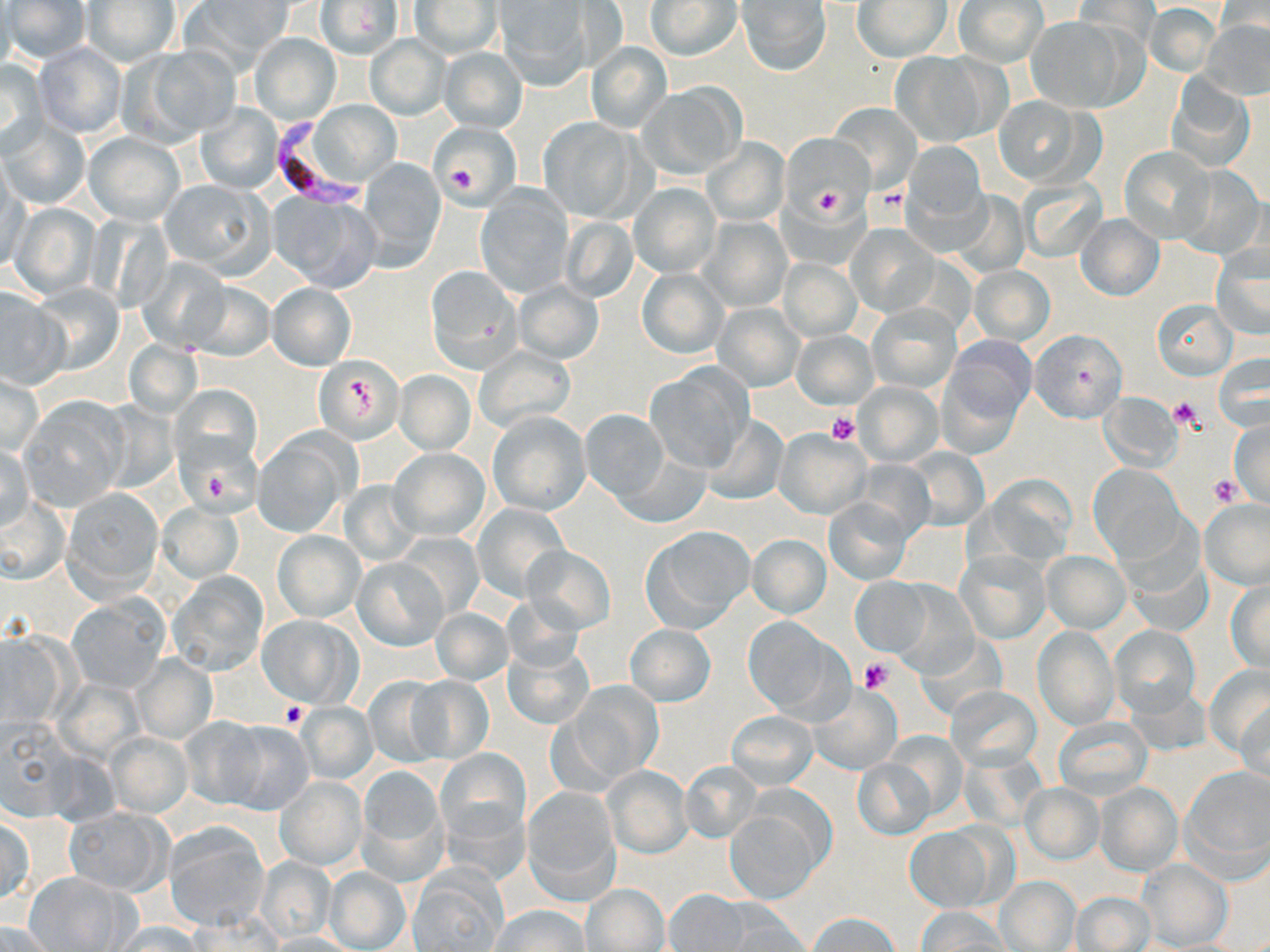 Approximate bounding boxes as [x1, y1, x2, y2] in pixels. Platelet locations: [447, 164, 477, 192], [811, 185, 846, 218], [872, 186, 910, 219], [348, 376, 373, 412], [1168, 396, 1203, 430], [826, 412, 860, 445], [203, 472, 230, 498], [1209, 474, 1243, 506], [859, 658, 893, 693], [280, 702, 308, 729]. Uninfected red blood cell locations: [5, 0, 90, 63], [186, 0, 295, 69], [645, 0, 741, 60], [737, 0, 831, 75], [315, 1, 405, 60], [409, 1, 503, 58], [494, 1, 589, 87], [853, 1, 953, 62], [953, 1, 1048, 67], [1072, 1, 1158, 60], [82, 2, 181, 67], [1144, 4, 1221, 76], [1025, 18, 1129, 112], [1201, 20, 1270, 100], [249, 34, 340, 126], [364, 35, 450, 120], [33, 42, 128, 139], [587, 42, 672, 132], [126, 46, 240, 143], [438, 48, 528, 132], [891, 50, 1006, 147], [1, 58, 49, 155], [1167, 75, 1256, 173], [637, 83, 747, 180], [993, 97, 1099, 188], [311, 101, 401, 187], [197, 103, 284, 194], [829, 106, 920, 191], [539, 117, 643, 221], [0, 119, 89, 210], [430, 121, 521, 204], [85, 132, 185, 225], [782, 134, 873, 219], [702, 136, 791, 226], [901, 141, 989, 236], [1119, 147, 1216, 243], [356, 158, 446, 270], [1169, 163, 1266, 262], [1, 171, 29, 276], [160, 179, 274, 276], [1017, 179, 1108, 261], [628, 182, 721, 279], [476, 189, 575, 298], [948, 190, 1030, 278], [269, 193, 380, 292], [8, 202, 101, 300], [1074, 214, 1164, 301], [699, 216, 793, 313], [559, 217, 639, 303], [846, 226, 940, 318], [1211, 243, 1270, 341], [136, 256, 230, 353], [779, 258, 861, 341], [969, 265, 1054, 346], [426, 267, 521, 373], [638, 269, 727, 358], [184, 280, 275, 361], [513, 281, 604, 363], [29, 282, 125, 375], [267, 282, 356, 371], [0, 286, 67, 389], [1151, 299, 1237, 379], [866, 302, 962, 394], [713, 304, 804, 391], [1028, 328, 1127, 424], [792, 331, 877, 408], [942, 335, 1036, 428], [124, 341, 202, 418], [472, 345, 577, 437], [1215, 355, 1267, 432], [314, 356, 404, 443], [644, 365, 753, 474], [394, 371, 475, 453], [0, 372, 42, 458], [854, 382, 942, 465], [1099, 391, 1182, 472], [24, 398, 126, 508], [580, 408, 670, 502], [486, 411, 590, 516], [701, 414, 788, 506], [1228, 419, 1270, 504], [774, 428, 872, 519], [253, 434, 352, 536], [1, 442, 34, 532], [614, 444, 710, 528], [902, 447, 988, 531], [388, 448, 489, 542], [1089, 465, 1185, 562], [978, 474, 1077, 567], [339, 480, 422, 566], [63, 488, 163, 596], [2, 494, 67, 583], [824, 497, 913, 584], [1198, 498, 1270, 590], [158, 502, 243, 583], [472, 503, 570, 600], [1114, 517, 1209, 634], [641, 527, 753, 631], [273, 530, 365, 622], [395, 532, 482, 620], [748, 534, 830, 618], [521, 545, 616, 634], [957, 549, 1050, 643], [1041, 550, 1130, 632], [352, 557, 447, 651], [167, 571, 269, 676], [850, 578, 932, 657], [1226, 579, 1270, 673], [68, 596, 168, 693], [431, 607, 513, 686], [257, 614, 361, 707], [742, 616, 851, 721], [626, 624, 715, 706], [1033, 626, 1119, 730], [1109, 626, 1199, 720], [503, 641, 593, 729], [132, 654, 216, 743], [1205, 665, 1269, 759], [362, 676, 450, 767], [405, 676, 493, 764], [562, 682, 663, 787], [810, 684, 902, 774], [947, 687, 1041, 770], [1235, 691, 1270, 784], [296, 702, 377, 784], [727, 710, 818, 788], [1052, 716, 1152, 801], [1, 717, 82, 818], [182, 718, 273, 808], [215, 719, 314, 816], [107, 733, 191, 817], [437, 748, 530, 842], [957, 750, 1046, 831], [852, 756, 936, 841], [679, 761, 763, 844], [604, 766, 692, 857], [1181, 766, 1268, 877], [356, 768, 444, 883], [276, 777, 366, 869], [1095, 781, 1184, 877], [522, 784, 621, 901], [1021, 784, 1102, 863], [725, 807, 822, 902], [65, 808, 170, 894], [1, 816, 34, 905], [165, 822, 270, 930], [905, 825, 1000, 913], [255, 858, 337, 941], [1136, 859, 1232, 951], [325, 867, 411, 952], [26, 871, 135, 951], [407, 873, 504, 951], [996, 877, 1081, 951], [582, 884, 669, 951], [665, 890, 753, 951], [1070, 892, 1155, 951], [702, 898, 807, 949], [492, 905, 589, 951], [916, 906, 1008, 951], [807, 911, 901, 951], [109, 921, 203, 952], [0, 922, 59, 952], [265, 932, 361, 952]. Plasmodium falciparum-infected red blood cell locations: [270, 118, 365, 209]. Slide-level diagnosis: Plasmodium falciparum. May-Grünwald-Giemsa-stained preparation. Optical microscopy. Image is 1270×952 pixels. Captured at 1000x magnification. Single field of view. Thin blood film.